Comment on the morphology of the erythrocytes.
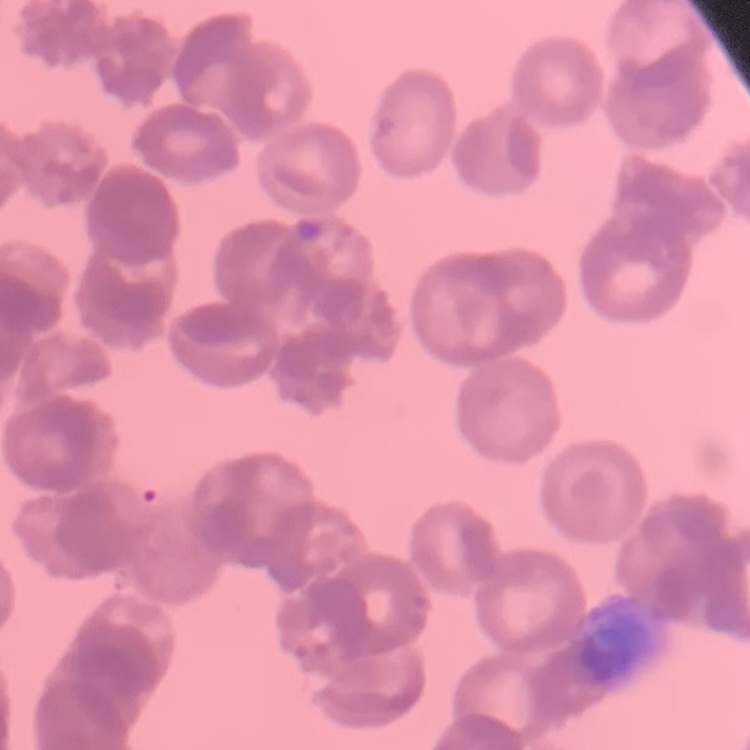
They show rouleaux formation.

stain: Field's or Giemsa
image_type: square crop of a larger photomicrograph
preparation: thin blood film